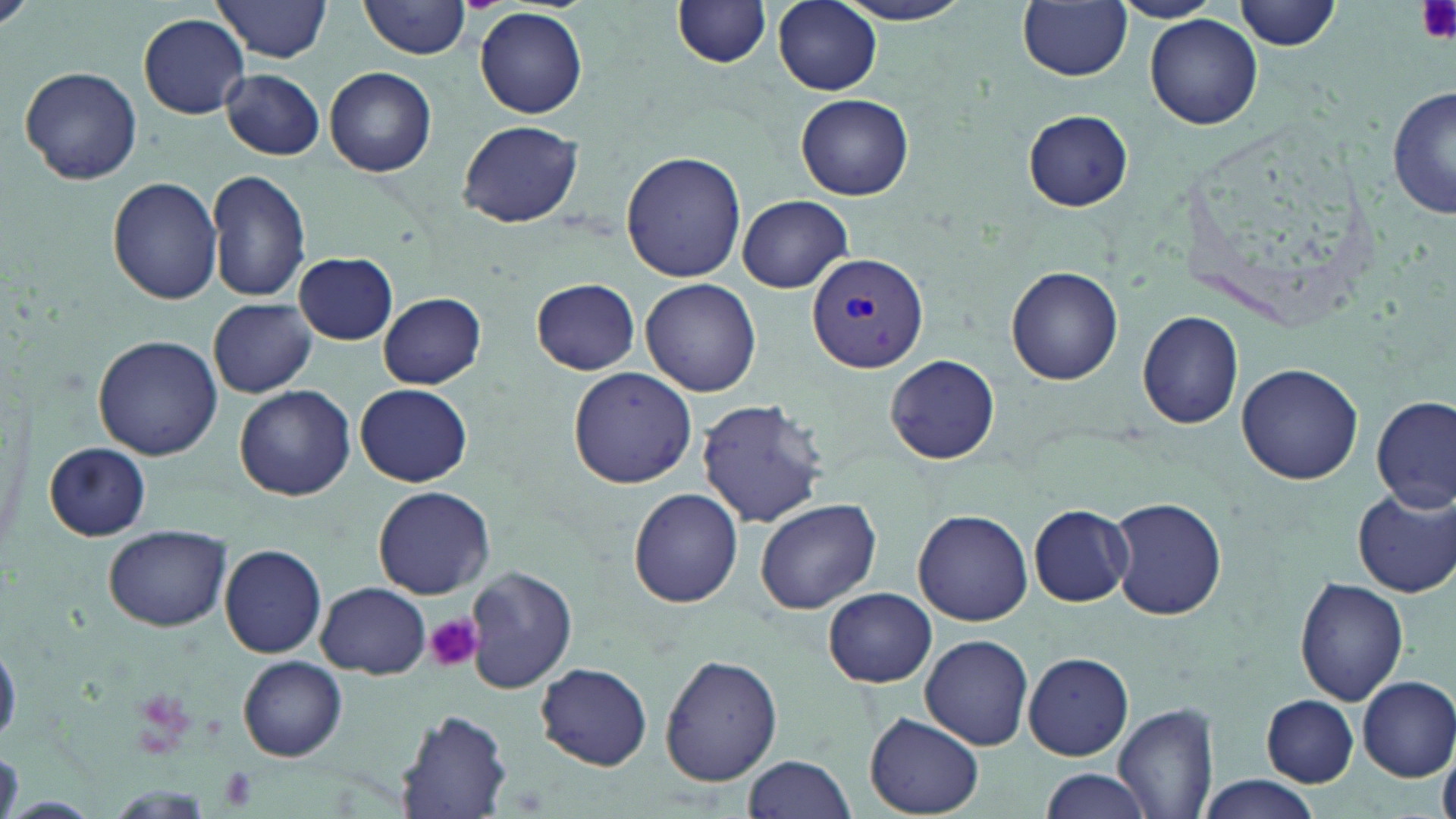

Summary:
  - Coordinate format: approximate bounding boxes as [x1, y1, x2, y2] in pixels
  - Uninfected red blood cell locations: [0, 0, 33, 33], [212, 0, 334, 62], [360, 0, 473, 58], [773, 0, 882, 95], [830, 0, 978, 25], [1113, 0, 1224, 23], [1234, 0, 1342, 50], [672, 1, 774, 68], [1019, 1, 1131, 82], [476, 8, 588, 118], [138, 13, 251, 119], [1145, 15, 1264, 130], [18, 65, 143, 185], [325, 66, 437, 177], [220, 69, 326, 160], [1389, 85, 1455, 221], [796, 94, 914, 201], [1024, 110, 1133, 210], [458, 120, 586, 229], [621, 151, 746, 283], [204, 170, 313, 302], [108, 176, 222, 305], [736, 196, 852, 291], [294, 254, 398, 345], [1006, 266, 1123, 385], [532, 277, 641, 376], [641, 278, 761, 398], [379, 292, 487, 389], [209, 299, 318, 398], [1137, 310, 1244, 429], [91, 334, 222, 463], [885, 355, 1000, 464], [1236, 361, 1365, 485], [567, 365, 697, 489], [355, 383, 472, 486], [234, 385, 356, 500], [1373, 396, 1455, 513], [697, 397, 829, 528], [45, 441, 153, 540], [373, 486, 494, 600], [1353, 486, 1456, 597], [629, 487, 742, 608], [1105, 495, 1227, 619], [754, 499, 881, 614], [1028, 506, 1132, 606], [913, 508, 1033, 625], [106, 524, 230, 631], [218, 544, 329, 658], [465, 566, 577, 693], [1295, 576, 1409, 705], [315, 582, 430, 678], [824, 587, 938, 688], [919, 634, 1033, 750], [0, 642, 21, 744], [1023, 652, 1135, 761], [660, 653, 782, 787], [237, 655, 348, 761], [533, 661, 653, 770], [1357, 676, 1456, 780], [1260, 694, 1360, 787], [1114, 702, 1220, 819], [396, 710, 514, 817], [865, 715, 985, 816], [742, 754, 858, 819], [1038, 769, 1154, 819], [1193, 775, 1324, 819], [1, 796, 103, 817]
  - Plasmodium vivax-infected red blood cell locations: [806, 251, 929, 372]
  - Platelet locations: [1416, 0, 1452, 44], [426, 614, 485, 674], [217, 765, 260, 813]
  - Slide-level diagnosis: Plasmodium vivax
  - Preparation: thin blood film
  - Modality: optical microscopy
  - Stain: May-Grünwald-Giemsa
  - Field of view: one of a larger specimen
  - Magnification: 1000x
  - Image size: 1456×819 pixels